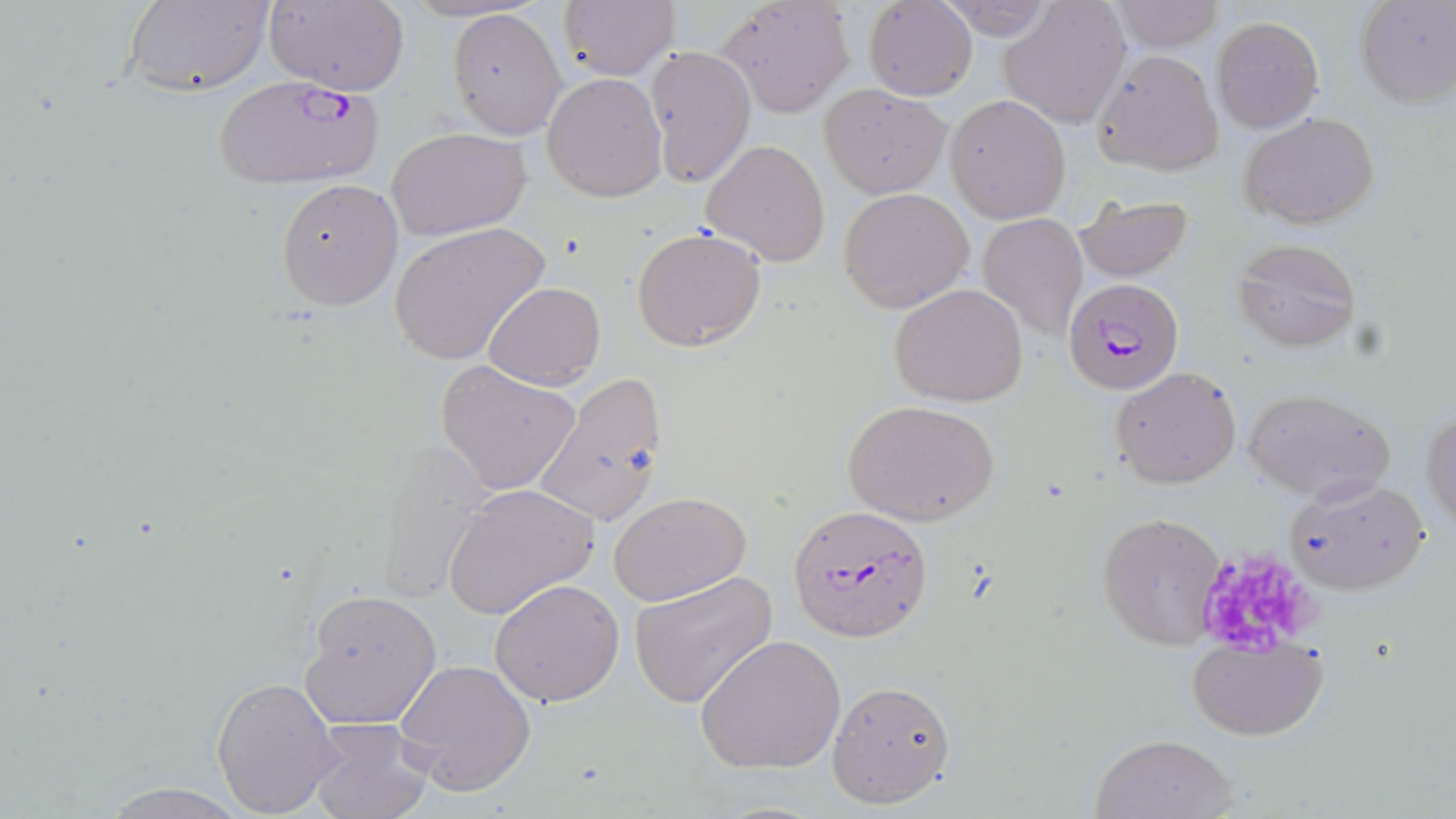

Approximate bounding boxes as [x1, y1, x2, y2] in pixels. Plasmodium falciparum-infected red blood cell locations: [210, 72, 385, 191], [1062, 277, 1185, 398], [796, 506, 941, 644]. Uninfected red blood cell locations: [122, 0, 273, 97], [266, 0, 410, 96], [557, 0, 679, 82], [714, 0, 857, 117], [935, 0, 1057, 40], [998, 0, 1131, 127], [1355, 0, 1456, 109], [864, 1, 976, 102], [1108, 1, 1223, 51], [447, 7, 566, 140], [1210, 15, 1326, 134], [645, 45, 756, 188], [1090, 50, 1225, 178], [542, 73, 667, 201], [820, 85, 950, 198], [946, 94, 1070, 223], [1239, 110, 1380, 229], [387, 128, 529, 241], [702, 139, 831, 266], [273, 179, 403, 311], [839, 187, 975, 313], [1073, 194, 1195, 283], [976, 212, 1086, 341], [389, 222, 549, 368], [631, 227, 766, 352], [1231, 237, 1361, 352], [482, 282, 605, 388], [890, 283, 1029, 407], [435, 360, 583, 496], [1110, 366, 1241, 488], [532, 373, 668, 527], [1243, 387, 1395, 504], [843, 399, 999, 525], [1421, 407, 1456, 531], [370, 440, 496, 601], [1284, 477, 1432, 595], [442, 482, 600, 621], [609, 492, 751, 606], [1095, 512, 1227, 650], [629, 572, 778, 709], [489, 578, 625, 705], [300, 589, 442, 730], [698, 635, 847, 775], [1186, 637, 1328, 740], [395, 657, 536, 795], [211, 675, 342, 816], [827, 679, 956, 807], [307, 718, 435, 819], [1090, 731, 1239, 819], [98, 783, 251, 817]. Platelet locations: [1203, 554, 1323, 658]. Slide-level diagnosis: Plasmodium falciparum. May-Grünwald-Giemsa-stained preparation. 1000x magnification. One field of a larger specimen. Light microscopy. Image is 1456×819 pixels. Thin blood film.